Locate every blood parasite and identify its species.
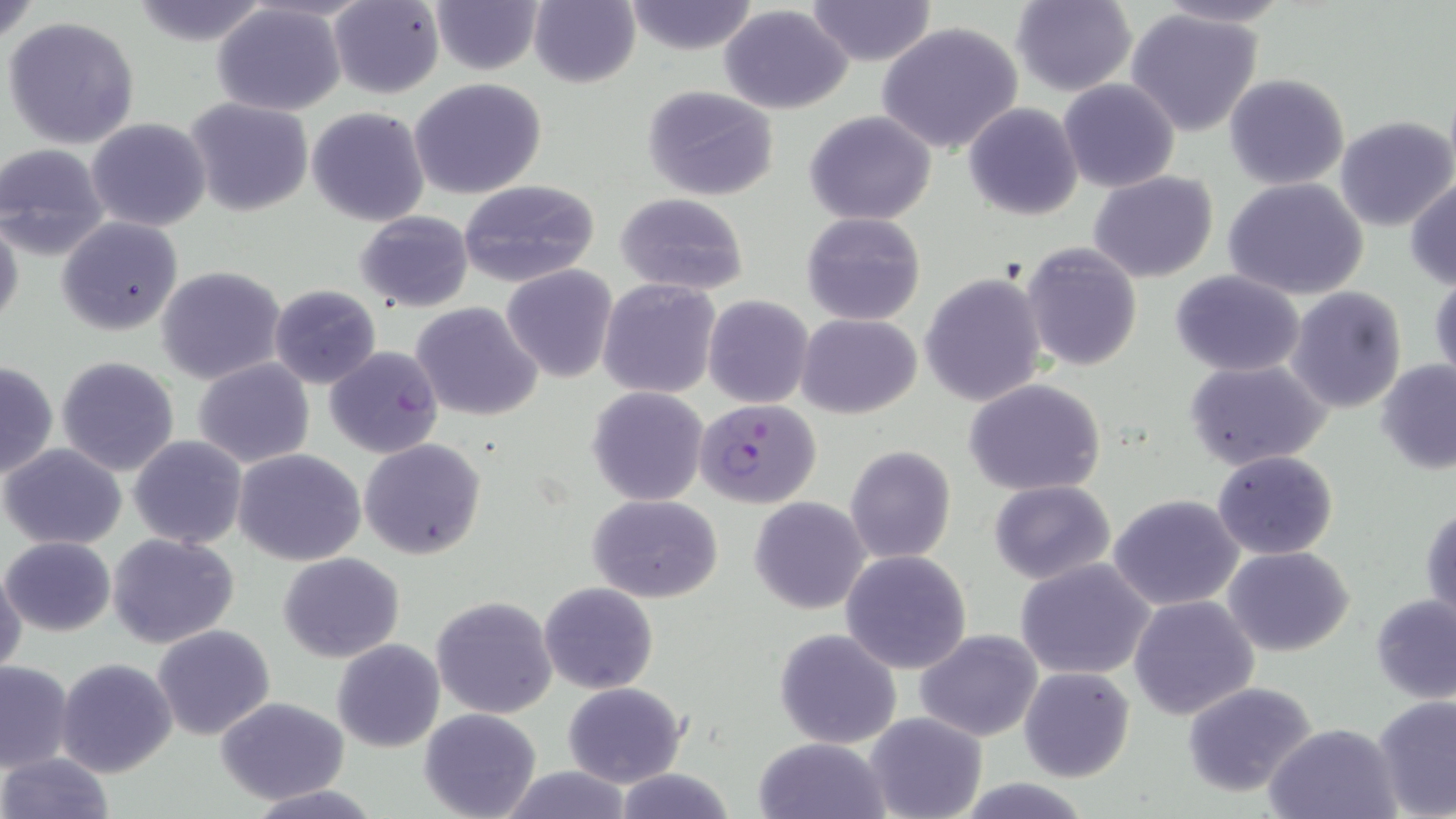

Approximate bounding boxes as (x1, y1, x2, y2) in pixels.
Plasmodium falciparum-infected red blood cells: (697, 398, 821, 509).
No Plasmodium ovale, Plasmodium malariae, Plasmodium vivax, Babesia divergens, or Trypanosoma brucei observed.

Summary:
  - Uninfected red blood cell locations: (129, 0, 273, 45), (428, 0, 546, 74), (530, 0, 642, 87), (806, 0, 935, 67), (1148, 0, 1295, 28), (0, 1, 42, 47), (328, 1, 445, 98), (624, 1, 759, 54), (1009, 1, 1137, 95), (211, 3, 346, 115), (719, 5, 854, 114), (1124, 8, 1266, 137), (5, 17, 141, 148), (877, 21, 1026, 156), (1224, 73, 1349, 190), (409, 78, 548, 200), (1058, 78, 1180, 192), (642, 86, 779, 202), (184, 97, 315, 217), (963, 102, 1084, 221), (306, 107, 430, 227), (804, 111, 937, 225), (1334, 115, 1455, 232), (86, 117, 212, 232), (0, 142, 110, 258), (1089, 172, 1218, 281), (1406, 173, 1456, 291), (458, 178, 600, 287), (1224, 178, 1369, 300), (615, 192, 749, 295), (353, 211, 474, 312), (801, 213, 926, 326), (0, 214, 24, 337), (56, 216, 184, 335), (997, 243, 1136, 485), (1020, 244, 1143, 371), (501, 264, 617, 382), (157, 266, 288, 386), (1171, 270, 1306, 376), (1429, 271, 1456, 388), (922, 272, 1045, 406), (598, 279, 723, 400), (269, 284, 381, 389), (1286, 287, 1407, 413), (704, 295, 814, 408), (412, 301, 544, 421), (797, 313, 921, 419), (326, 346, 444, 459), (56, 355, 180, 474), (1, 359, 58, 480), (192, 359, 316, 468), (1185, 359, 1330, 469), (1374, 359, 1456, 475), (964, 379, 1106, 496), (587, 386, 709, 507), (128, 435, 248, 550), (359, 438, 486, 560), (1, 443, 127, 548), (846, 445, 957, 564), (234, 449, 365, 565), (1213, 449, 1339, 560), (988, 480, 1116, 585), (1108, 493, 1245, 610), (587, 494, 724, 603), (749, 497, 871, 615), (1420, 500, 1455, 629), (108, 532, 240, 647), (2, 536, 116, 636), (1224, 546, 1354, 657), (841, 549, 972, 674), (278, 552, 404, 661), (1015, 558, 1156, 679), (0, 563, 26, 675), (539, 581, 657, 694), (431, 594, 559, 720), (1370, 594, 1456, 704), (1128, 596, 1260, 719), (151, 625, 276, 741), (775, 627, 902, 749), (915, 630, 1043, 743), (333, 639, 444, 753), (55, 657, 178, 777), (0, 660, 73, 772), (1019, 666, 1136, 782), (562, 681, 687, 787), (1180, 681, 1319, 797), (214, 695, 351, 804), (1371, 695, 1456, 819), (419, 706, 541, 819), (865, 712, 987, 819), (1264, 721, 1402, 819), (753, 738, 890, 819), (0, 753, 115, 819), (495, 765, 639, 819), (610, 766, 737, 819), (955, 779, 1096, 817), (244, 785, 384, 819)
  - Slide-level diagnosis: Plasmodium falciparum
  - Field of view: single
  - Stain: May-Grünwald-Giemsa
  - Modality: optical microscopy
  - Magnification: 1000x
  - Preparation: thin blood film
  - Image size: 1456×819 pixels